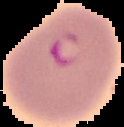

From a thin blood smear. Malaria status: parasitized. Image is 124×127 pixels. Segmented cell region on a black background.